Classify the preparation.
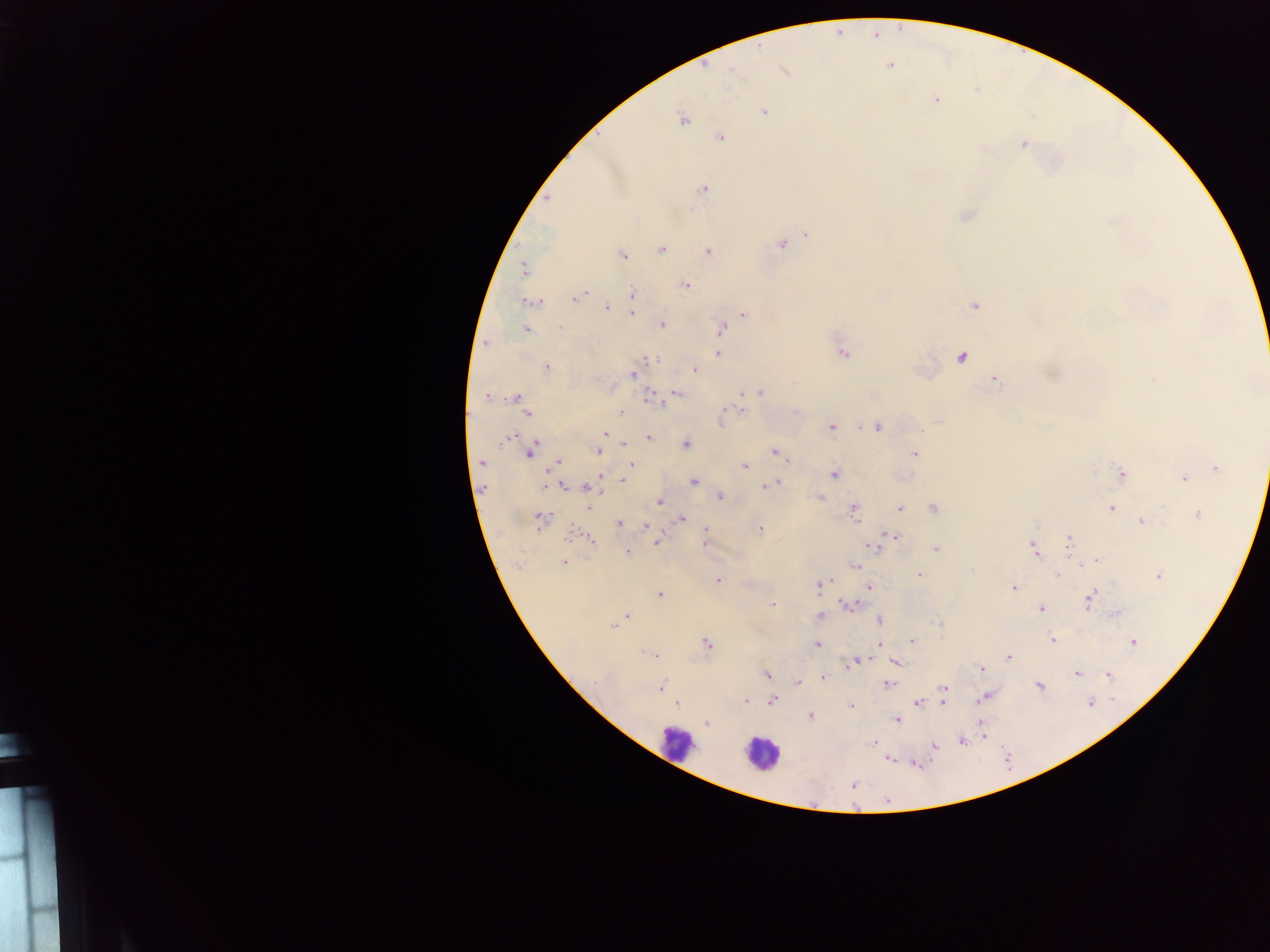

Thick blood smear.

Approximate centers as {x, y} in pixels.
Summary:
  - Leukocyte locations: {676, 742}, {761, 754}
  - Malaria parasite locations: {875, 36}, {889, 65}, {784, 70}, {936, 100}, {764, 111}, {682, 119}, {720, 137}, {1024, 144}, {703, 189}, {807, 235}, {781, 244}, {662, 248}, {709, 252}, {622, 255}, {524, 268}, {685, 285}, {582, 293}, {632, 293}, {577, 298}, {532, 301}, {975, 305}, {606, 307}, {632, 314}, {743, 314}, {661, 324}, {559, 326}, {526, 329}, {720, 329}, {718, 353}, {843, 353}, {961, 357}, {651, 359}, {546, 367}, {694, 370}, {633, 374}, {996, 381}, {677, 392}, {743, 393}, {760, 393}, {486, 397}, {516, 397}, {651, 397}, {742, 410}, {621, 412}, {527, 413}, {940, 421}, {720, 423}, {831, 427}, {877, 427}, {606, 434}, {649, 437}, {509, 438}, {623, 443}, {686, 444}, {600, 447}, {533, 448}, {597, 451}, {775, 452}, {529, 453}, {914, 453}, {481, 462}, {558, 462}, {631, 464}, {744, 466}, {1217, 468}, {1122, 474}, {834, 475}, {599, 476}, {625, 477}, {1183, 478}, {623, 481}, {694, 482}, {776, 483}, {769, 485}, {564, 486}, {587, 487}, {719, 496}, {820, 497}, {659, 502}, {589, 508}, {933, 508}, {900, 509}, {1111, 509}, {854, 510}, {1197, 515}, {540, 518}, {681, 518}, {1141, 521}, {619, 523}, {646, 526}, {706, 528}, {760, 529}, {894, 536}, {591, 539}, {1069, 539}, {656, 543}, {704, 544}, {874, 546}, {1034, 548}, {936, 549}, {627, 552}, {1096, 561}, {564, 562}, {856, 565}, {920, 575}, {1057, 575}, {1159, 576}, {718, 580}, {826, 581}, {821, 585}, {1014, 587}, {869, 588}, {660, 594}, {1089, 599}, {772, 604}, {847, 605}, {1041, 609}, {1116, 613}, {628, 616}, {822, 616}, {879, 620}, {613, 626}, {1053, 639}, {912, 640}, {706, 643}, {1133, 643}, {817, 644}, {879, 644}, {645, 651}, {653, 654}, {1009, 657}, {856, 662}, {894, 662}, {850, 665}, {981, 668}, {1077, 673}, {1108, 674}, {767, 675}, {823, 678}, {798, 683}, {888, 683}, {1039, 686}, {661, 687}, {945, 688}, {985, 697}, {746, 700}, {773, 700}, {942, 702}, {1090, 702}, {918, 703}, {677, 704}, {851, 705}, {810, 716}, {897, 719}, {706, 722}, {981, 725}, {962, 741}, {874, 743}, {934, 746}, {888, 759}, {853, 785}, {887, 800}
  - Field of view: single
  - Image size: 1270×952 pixels
  - Country: Ghana
  - Capture: mobile-phone photograph through a microscope